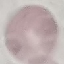

Result: negative for malaria parasites. Thin smear of blood. Giemsa stain. Acquired by smartphone through the microscope eyepiece. Automatically extracted cell patch, resized to 64 × 64 pixels.